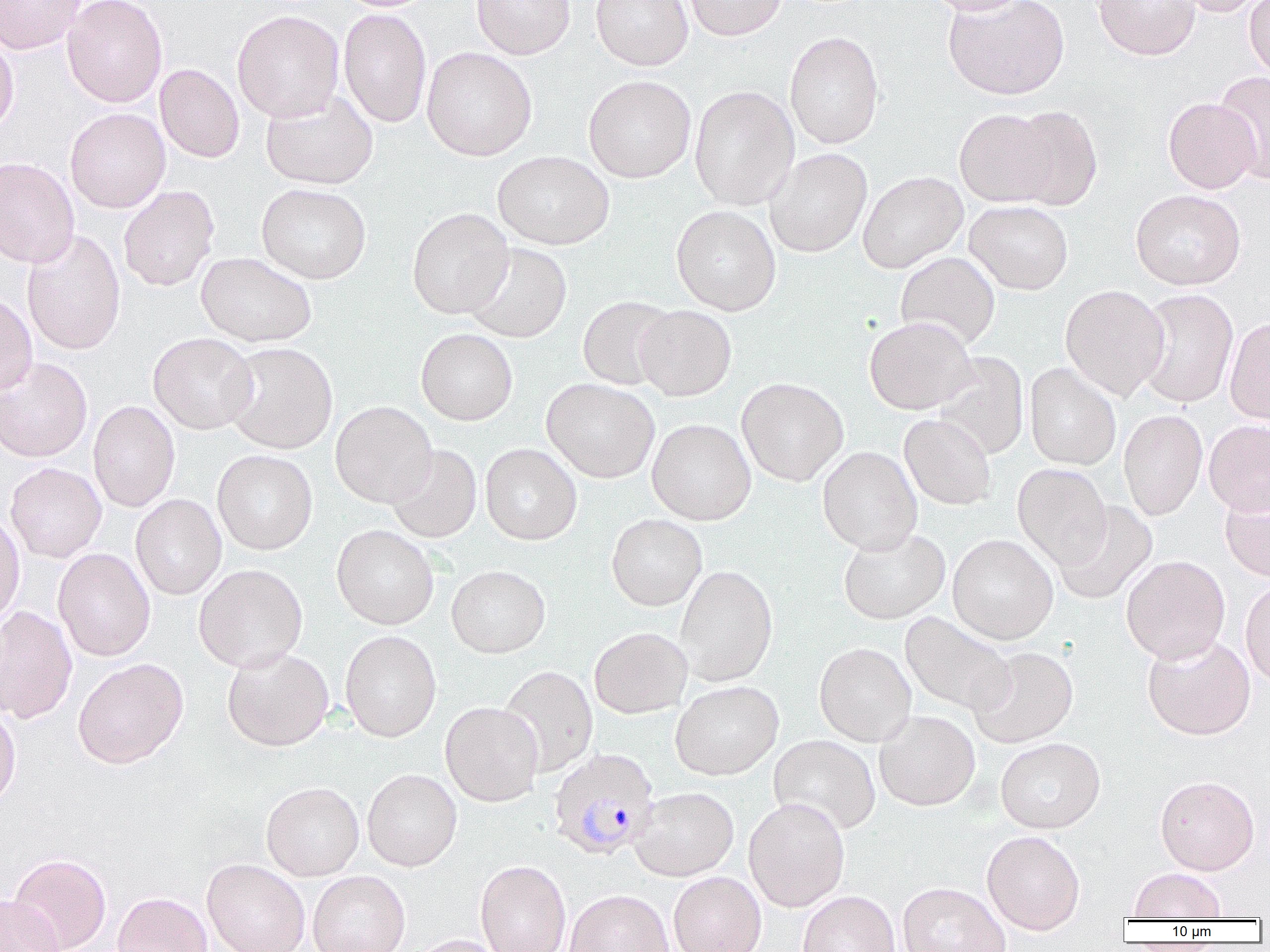

Plasmodium malariae-infected red blood cell locations = approximate bounding boxes as named x1/y1/x2/y2 corners in pixels: (x1=548, y1=748, x2=659, y2=860)
slide-level diagnosis = Plasmodium malariae
uninfected red blood cell locations = approximate bounding boxes as named x1/y1/x2/y2 corners in pixels: (x1=0, y1=0, x2=85, y2=54), (x1=62, y1=0, x2=167, y2=107), (x1=472, y1=0, x2=575, y2=60), (x1=591, y1=0, x2=693, y2=70), (x1=684, y1=0, x2=787, y2=40), (x1=922, y1=0, x2=1028, y2=15), (x1=943, y1=0, x2=1069, y2=100), (x1=1094, y1=0, x2=1200, y2=60), (x1=1176, y1=0, x2=1266, y2=17), (x1=1244, y1=0, x2=1270, y2=79), (x1=339, y1=8, x2=432, y2=128), (x1=232, y1=9, x2=344, y2=122), (x1=0, y1=31, x2=19, y2=137), (x1=784, y1=31, x2=884, y2=149), (x1=421, y1=47, x2=537, y2=161), (x1=155, y1=64, x2=244, y2=163), (x1=1214, y1=72, x2=1270, y2=184), (x1=583, y1=75, x2=696, y2=182), (x1=689, y1=85, x2=799, y2=210), (x1=260, y1=90, x2=378, y2=189), (x1=1163, y1=97, x2=1260, y2=194), (x1=1005, y1=106, x2=1102, y2=211), (x1=65, y1=108, x2=170, y2=213), (x1=954, y1=108, x2=1057, y2=207), (x1=765, y1=148, x2=872, y2=258), (x1=492, y1=150, x2=614, y2=250), (x1=0, y1=156, x2=80, y2=268), (x1=858, y1=171, x2=967, y2=273), (x1=256, y1=183, x2=372, y2=284), (x1=118, y1=186, x2=219, y2=291), (x1=1130, y1=189, x2=1246, y2=290), (x1=965, y1=201, x2=1073, y2=294), (x1=671, y1=205, x2=782, y2=316), (x1=407, y1=208, x2=513, y2=318), (x1=21, y1=229, x2=126, y2=355), (x1=463, y1=242, x2=572, y2=343), (x1=196, y1=251, x2=317, y2=347), (x1=895, y1=252, x2=1000, y2=351), (x1=1060, y1=284, x2=1170, y2=400), (x1=1134, y1=288, x2=1239, y2=408), (x1=0, y1=293, x2=37, y2=396), (x1=578, y1=295, x2=677, y2=390), (x1=635, y1=305, x2=736, y2=401), (x1=864, y1=316, x2=977, y2=414), (x1=1224, y1=317, x2=1270, y2=425), (x1=416, y1=328, x2=518, y2=425), (x1=148, y1=332, x2=258, y2=434), (x1=223, y1=342, x2=338, y2=454), (x1=932, y1=352, x2=1029, y2=459), (x1=0, y1=356, x2=92, y2=463), (x1=1024, y1=362, x2=1121, y2=470), (x1=737, y1=377, x2=848, y2=486), (x1=542, y1=378, x2=660, y2=482), (x1=88, y1=400, x2=180, y2=512), (x1=331, y1=401, x2=437, y2=507), (x1=1118, y1=409, x2=1207, y2=520), (x1=899, y1=414, x2=996, y2=509), (x1=647, y1=418, x2=756, y2=526), (x1=1204, y1=420, x2=1270, y2=516), (x1=481, y1=443, x2=581, y2=545), (x1=387, y1=445, x2=482, y2=543), (x1=817, y1=446, x2=922, y2=554), (x1=212, y1=450, x2=318, y2=554), (x1=5, y1=462, x2=106, y2=562), (x1=1012, y1=463, x2=1111, y2=568), (x1=1220, y1=481, x2=1270, y2=581), (x1=131, y1=494, x2=227, y2=600), (x1=1053, y1=501, x2=1157, y2=604), (x1=0, y1=510, x2=25, y2=627), (x1=607, y1=514, x2=707, y2=610), (x1=332, y1=524, x2=439, y2=629), (x1=838, y1=527, x2=950, y2=624), (x1=948, y1=534, x2=1058, y2=644), (x1=53, y1=548, x2=155, y2=661), (x1=1121, y1=555, x2=1230, y2=664), (x1=194, y1=564, x2=308, y2=672), (x1=446, y1=565, x2=551, y2=658), (x1=675, y1=565, x2=778, y2=686), (x1=1240, y1=579, x2=1270, y2=688), (x1=0, y1=606, x2=77, y2=723), (x1=899, y1=611, x2=1015, y2=715), (x1=589, y1=626, x2=692, y2=718), (x1=340, y1=630, x2=441, y2=742), (x1=1142, y1=634, x2=1256, y2=740), (x1=815, y1=642, x2=916, y2=747), (x1=222, y1=646, x2=334, y2=751), (x1=968, y1=646, x2=1078, y2=748), (x1=73, y1=657, x2=188, y2=769), (x1=499, y1=665, x2=598, y2=776), (x1=670, y1=680, x2=784, y2=780), (x1=440, y1=701, x2=543, y2=807), (x1=0, y1=704, x2=21, y2=811), (x1=874, y1=710, x2=980, y2=811), (x1=768, y1=735, x2=881, y2=834), (x1=995, y1=737, x2=1106, y2=833), (x1=362, y1=768, x2=462, y2=871), (x1=1154, y1=775, x2=1260, y2=874), (x1=261, y1=781, x2=364, y2=880), (x1=630, y1=787, x2=739, y2=881), (x1=744, y1=797, x2=850, y2=912), (x1=982, y1=830, x2=1086, y2=934), (x1=8, y1=853, x2=111, y2=952), (x1=202, y1=858, x2=310, y2=952), (x1=475, y1=858, x2=571, y2=952), (x1=1128, y1=867, x2=1227, y2=920), (x1=308, y1=870, x2=410, y2=952), (x1=668, y1=872, x2=766, y2=952), (x1=897, y1=881, x2=1010, y2=952), (x1=564, y1=888, x2=674, y2=952), (x1=798, y1=890, x2=900, y2=952), (x1=112, y1=892, x2=212, y2=952), (x1=0, y1=893, x2=65, y2=952), (x1=408, y1=934, x2=507, y2=952)
image size = 1270×952 pixels
preparation = thin blood film
modality = light microscopy
magnification = 1000x
field of view = single